Assess the morphology of the red blood cells.
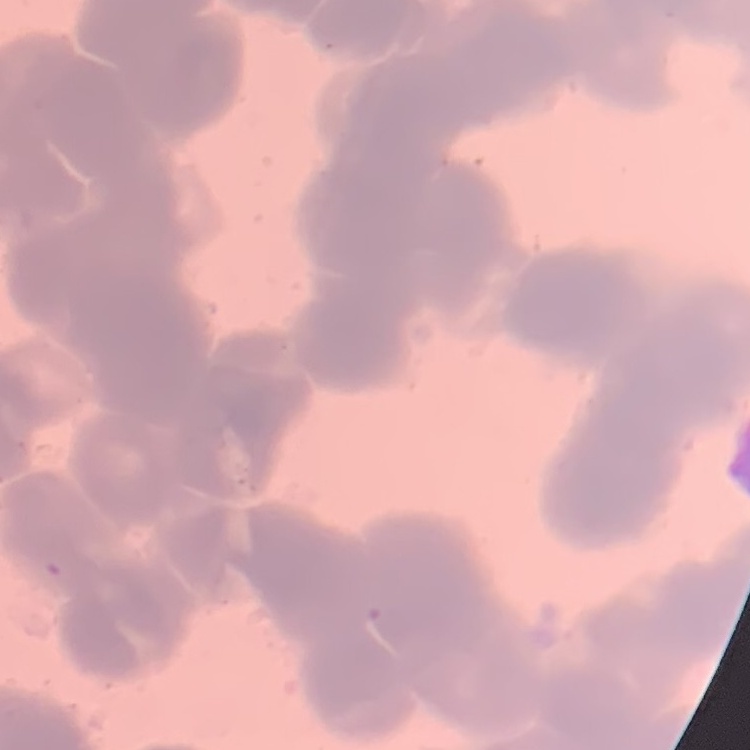

They show rouleaux formation.

image_type: square crop of a larger photomicrograph
preparation: thin blood smear
stain: Field's or Giemsa